Comment on the morphology of the red blood cells.
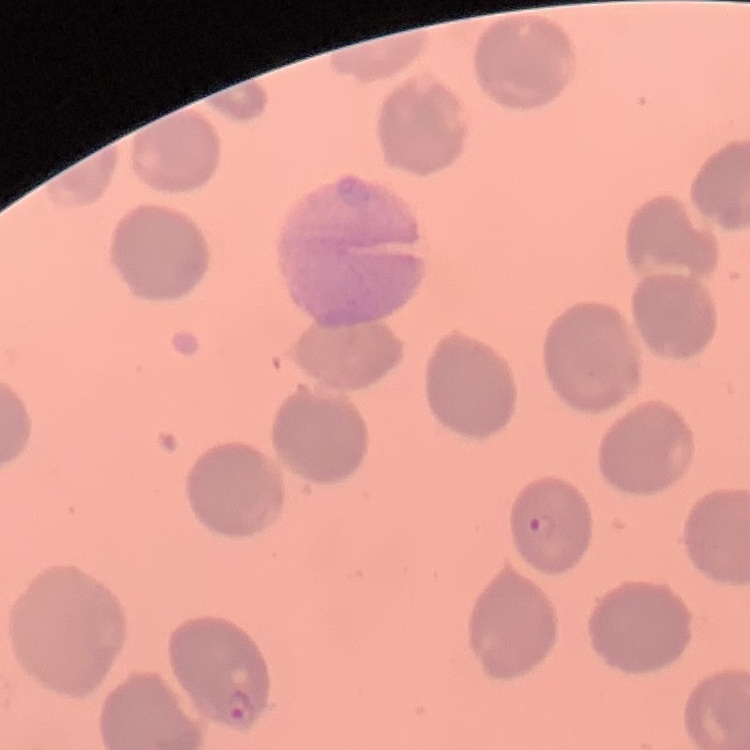

No rouleaux formation.

Summary:
  - Image type: square crop of a larger photomicrograph
  - Preparation: thin blood film
  - Stain: Field's or Giemsa